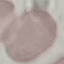
Summary:
  - Malaria status: uninfected
  - Capture: smartphone through the microscope eyepiece
  - Stain: Giemsa
  - Image type: cell patch, automatically extracted from a larger field of view and resized to 64 × 64 pixels
  - Preparation: thin blood film